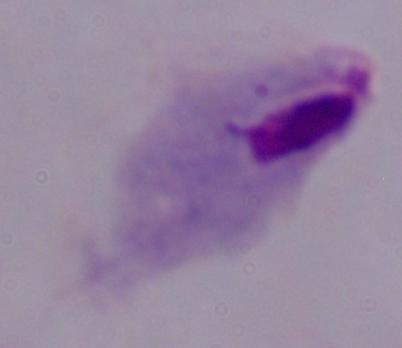
modality = photomicrograph
magnification = 1000x
identification = trichomonad